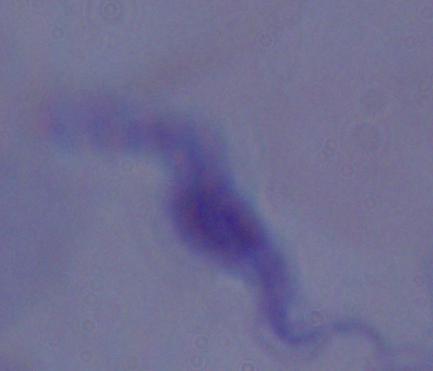
Micrograph. 1000x magnification. A trypanosome is seen.